Assess this cell for malaria.
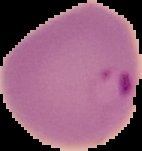
Parasitized.

Summary:
  - Image size: 142×151 pixels
  - Preparation: thin blood film
  - Image type: segmented cell region with the area outside set to black